Name the cell type shown.
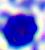
This is a leukocyte.

Summary:
  - Modality: photomicrograph
  - Magnification: 400x